Give the extent of all uninfected red blood cells.
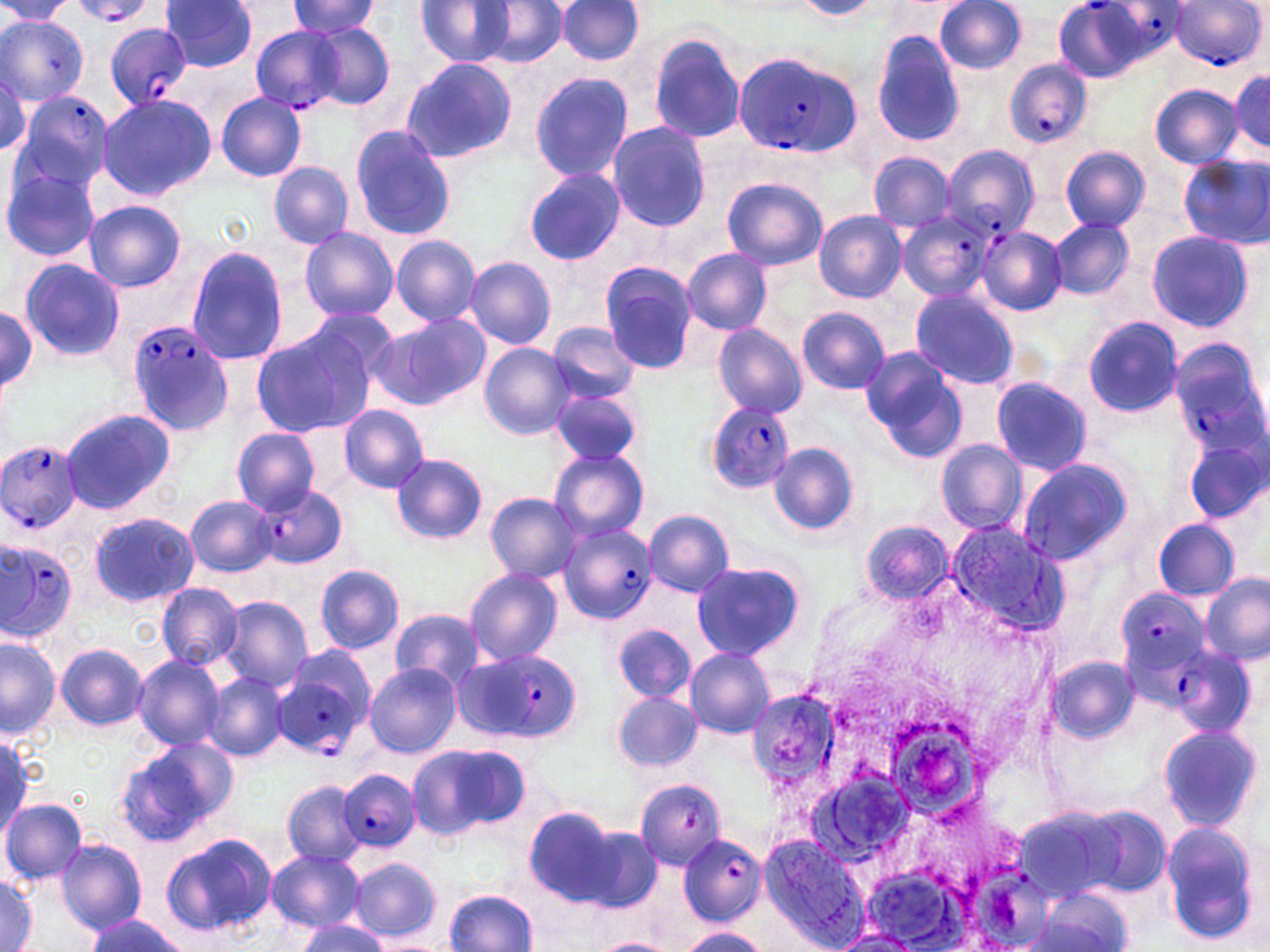
Approximate bounding boxes as [x1, y1, x2, y2] in pixels.
Uninfected red blood cells: [160, 0, 260, 72], [418, 0, 513, 65], [794, 0, 880, 20], [935, 0, 1026, 74], [0, 1, 74, 27], [286, 1, 382, 39], [478, 1, 567, 68], [557, 1, 645, 67], [0, 15, 90, 104], [309, 24, 395, 109], [646, 30, 747, 145], [869, 30, 966, 149], [401, 57, 515, 164], [529, 70, 634, 182], [1231, 71, 1269, 153], [1189, 77, 1270, 165], [1149, 84, 1242, 168], [215, 93, 308, 182], [95, 94, 216, 202], [607, 122, 709, 232], [349, 126, 455, 239], [1060, 147, 1149, 232], [868, 152, 955, 232], [1180, 155, 1269, 250], [268, 162, 353, 248], [1, 163, 101, 261], [524, 166, 625, 266], [722, 177, 827, 270], [84, 200, 187, 293], [813, 211, 907, 303], [1049, 217, 1133, 299], [300, 226, 398, 324], [1147, 230, 1253, 331], [391, 236, 482, 326], [186, 247, 288, 366], [683, 249, 772, 334], [464, 256, 555, 350], [18, 257, 125, 362], [600, 261, 699, 369], [911, 286, 1021, 390], [0, 304, 38, 394], [301, 306, 402, 385], [796, 307, 890, 394], [374, 315, 488, 408], [1083, 316, 1183, 418], [546, 323, 640, 405], [713, 323, 807, 420], [249, 330, 370, 440], [480, 343, 576, 440], [861, 348, 968, 464], [992, 377, 1091, 477], [549, 387, 641, 465], [339, 405, 431, 494], [60, 407, 176, 514], [231, 428, 322, 513], [1184, 434, 1268, 529], [935, 439, 1028, 536], [770, 442, 859, 535], [548, 447, 650, 543], [390, 454, 486, 544], [1016, 457, 1136, 566], [485, 492, 582, 583], [184, 494, 277, 578], [643, 509, 735, 596], [89, 511, 199, 608], [1153, 518, 1240, 600], [860, 520, 953, 605], [690, 560, 805, 661], [314, 564, 405, 653], [465, 568, 564, 666], [1201, 573, 1270, 665], [155, 582, 245, 669], [221, 597, 314, 690], [391, 608, 483, 689], [614, 625, 695, 702], [0, 636, 60, 738], [56, 642, 149, 732], [685, 646, 775, 738], [132, 654, 226, 751], [1047, 656, 1138, 744], [365, 664, 461, 756], [202, 673, 289, 762], [612, 691, 703, 773], [1156, 721, 1263, 832], [0, 731, 32, 834], [118, 737, 237, 845], [409, 743, 527, 839], [811, 766, 917, 870], [279, 778, 369, 868], [634, 779, 727, 868], [0, 798, 87, 883], [1075, 804, 1174, 898], [525, 806, 617, 902], [1159, 820, 1263, 947], [568, 822, 662, 914], [161, 833, 277, 937], [760, 834, 871, 951], [55, 838, 147, 934], [265, 849, 366, 932], [349, 857, 441, 941], [1, 873, 36, 952], [1039, 887, 1135, 952], [445, 890, 538, 951], [85, 915, 186, 952], [296, 918, 387, 952], [675, 927, 769, 952], [833, 930, 921, 951], [594, 937, 674, 952].

Summary:
  - Plasmodium falciparum-infected red blood cell locations: [1091, 0, 1187, 65], [66, 1, 159, 26], [1171, 2, 1264, 72], [102, 23, 190, 109], [249, 25, 350, 113], [732, 50, 863, 157], [1004, 60, 1093, 149], [10, 90, 115, 197], [943, 145, 1039, 238], [898, 213, 995, 302], [978, 227, 1067, 315], [124, 319, 234, 436], [1169, 339, 1268, 458], [708, 401, 792, 494], [0, 438, 84, 536], [257, 484, 348, 568], [559, 525, 656, 624], [0, 537, 79, 645], [1116, 588, 1209, 683], [1173, 643, 1258, 738], [460, 649, 580, 742], [274, 655, 374, 757], [341, 768, 420, 855], [677, 834, 768, 923]
  - Slide-level diagnosis: Plasmodium falciparum
  - Field of view: one of a larger specimen
  - Image size: 1270×952 pixels
  - Modality: light microscopy
  - Preparation: thin blood film
  - Stain: May-Grünwald-Giemsa
  - Magnification: 1000x